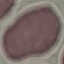

Summary:
  - Result: negative for malaria parasites
  - Stain: Giemsa
  - Preparation: thin blood smear
  - Image type: cell patch, automatically extracted from a larger field of view and resized to 64 × 64 pixels
  - Capture: smartphone camera at the microscope eyepiece